Give a bounding box for every parasitised red blood cell.
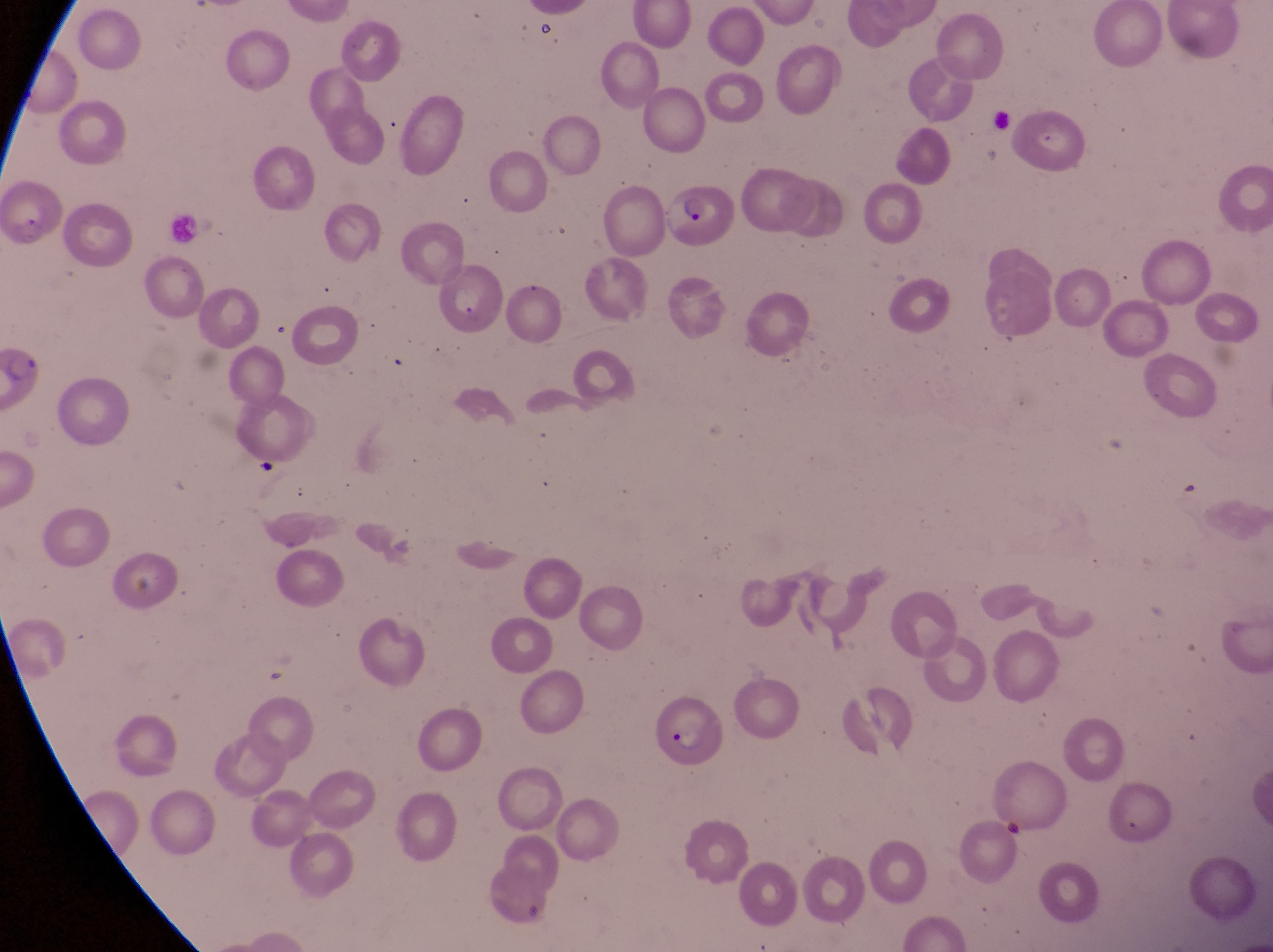

Approximate bounding boxes as {left, top, right, bottom} in pixels.
Parasitised red blood cells: {2, 174, 65, 254}, {661, 185, 739, 250}, {651, 692, 726, 766}.

Summary:
  - Field of view: single
  - Preparation: thin blood smear
  - Country: Uganda
  - Magnification: 1000x
  - Capture: smartphone photograph through the eyepiece of an Olympus CX-23 microscope
  - Image size: 1273×952 pixels